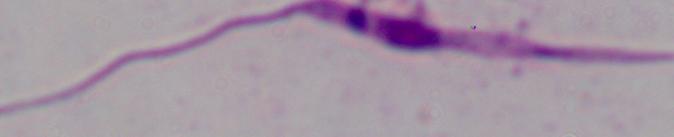

identification = Leishmania
modality = photomicrograph
magnification = 1000x